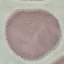
malaria status = uninfected
stain = Giemsa
image type = cell patch, automatically extracted from a larger field of view and resized to 64 × 64 pixels
preparation = thin blood smear
capture = smartphone camera at the microscope eyepiece